Identify the cell.
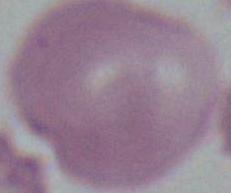
An erythrocyte.

magnification: 1000x
modality: photomicrograph